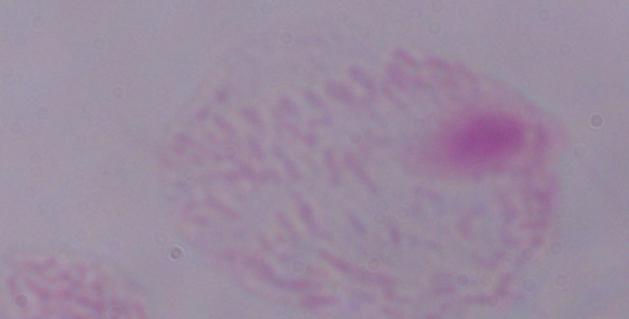
Summary:
  - Identification: trichomonad
  - Magnification: 1000x
  - Modality: photomicrograph